Name the blood parasite species.
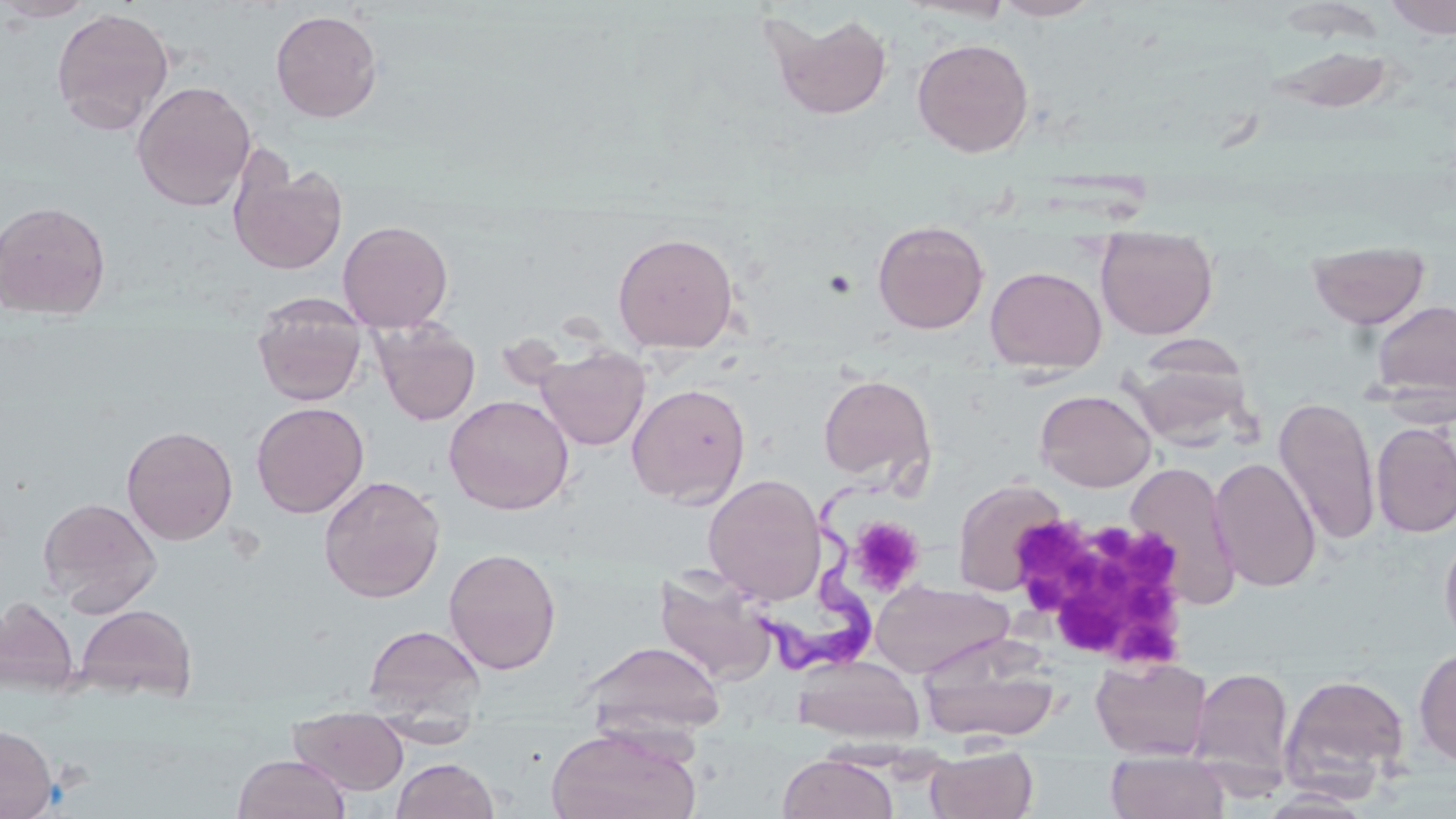
Trypanosoma brucei.

Summary:
  - Coordinate format: approximate bounding boxes as [x1, y1, x2, y2] in pixels
  - Platelet locations: [1025, 516, 1196, 670], [847, 517, 925, 597]
  - Trypanosoma brucei locations: [755, 485, 874, 676]
  - Uninfected red blood cell locations: [1, 0, 97, 22], [991, 0, 1103, 21], [1383, 0, 1455, 39], [50, 6, 175, 134], [270, 9, 383, 122], [762, 10, 894, 120], [912, 38, 1034, 158], [1265, 44, 1398, 114], [131, 80, 257, 211], [229, 154, 347, 275], [0, 200, 112, 321], [337, 219, 453, 331], [872, 219, 990, 334], [1096, 226, 1218, 340], [612, 231, 740, 354], [1307, 240, 1430, 329], [985, 266, 1107, 373], [252, 293, 368, 407], [1370, 299, 1456, 403], [372, 320, 480, 425], [535, 345, 651, 451], [1127, 346, 1255, 447], [818, 374, 936, 484], [626, 383, 751, 507], [1035, 388, 1157, 492], [444, 394, 574, 514], [1273, 396, 1381, 545], [251, 401, 369, 518], [1372, 422, 1456, 537], [121, 424, 238, 545], [1209, 457, 1322, 591], [1125, 461, 1241, 609], [702, 473, 826, 606], [318, 475, 445, 603], [951, 478, 1069, 597], [37, 496, 162, 615], [1439, 521, 1456, 652], [443, 547, 562, 674], [654, 564, 778, 684], [870, 579, 1013, 679], [0, 596, 79, 694], [74, 604, 198, 701], [363, 623, 486, 722], [917, 635, 1062, 744], [581, 640, 726, 739], [1413, 647, 1456, 768], [793, 655, 925, 745], [1090, 656, 1212, 760], [1188, 667, 1295, 789], [1280, 674, 1410, 792], [289, 707, 409, 795], [373, 717, 480, 748], [0, 724, 57, 819], [546, 726, 700, 819], [926, 747, 1038, 819], [1106, 752, 1229, 819], [233, 753, 350, 818], [778, 753, 898, 819], [390, 758, 500, 818], [1258, 789, 1374, 817]
  - Image size: 1456×819 pixels
  - Field of view: one of a larger specimen
  - Magnification: 1000x
  - Stain: May-Grünwald-Giemsa
  - Modality: light microscopy
  - Preparation: thin blood smear